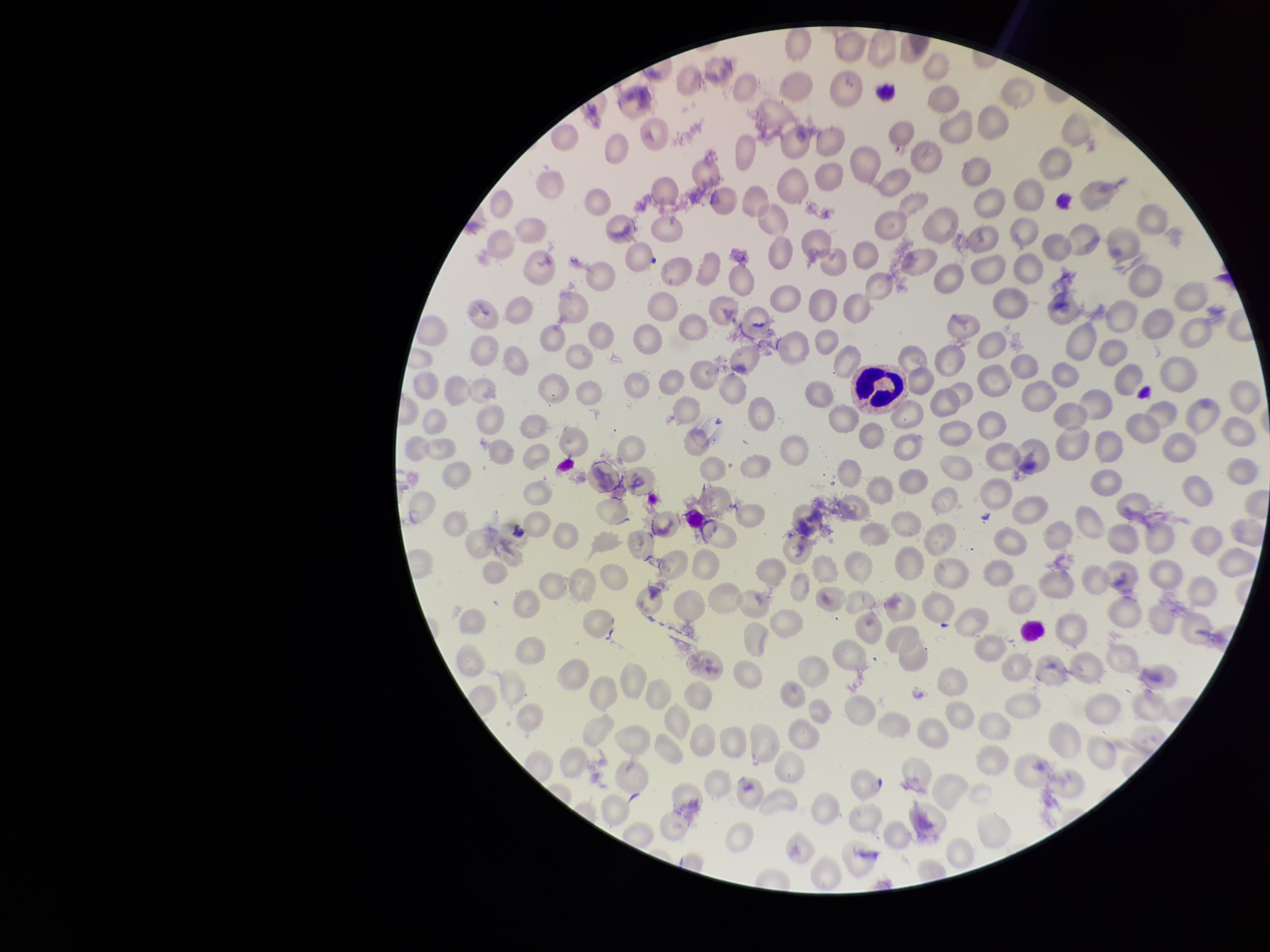

image_size: 1270×952 pixels
capture: smartphone photograph through the microscope eyepiece
parasitized_red_blood_cell_count: 0
preparation: thin blood smear
parasitized_red_blood_cells: none detected
stain: Giemsa
red_blood_cell_count: 213
field_of_view: single
species_reported_for_this_patient: Plasmodium vivax
patient_malaria_status: infected